Locate every blood parasite and identify its species.
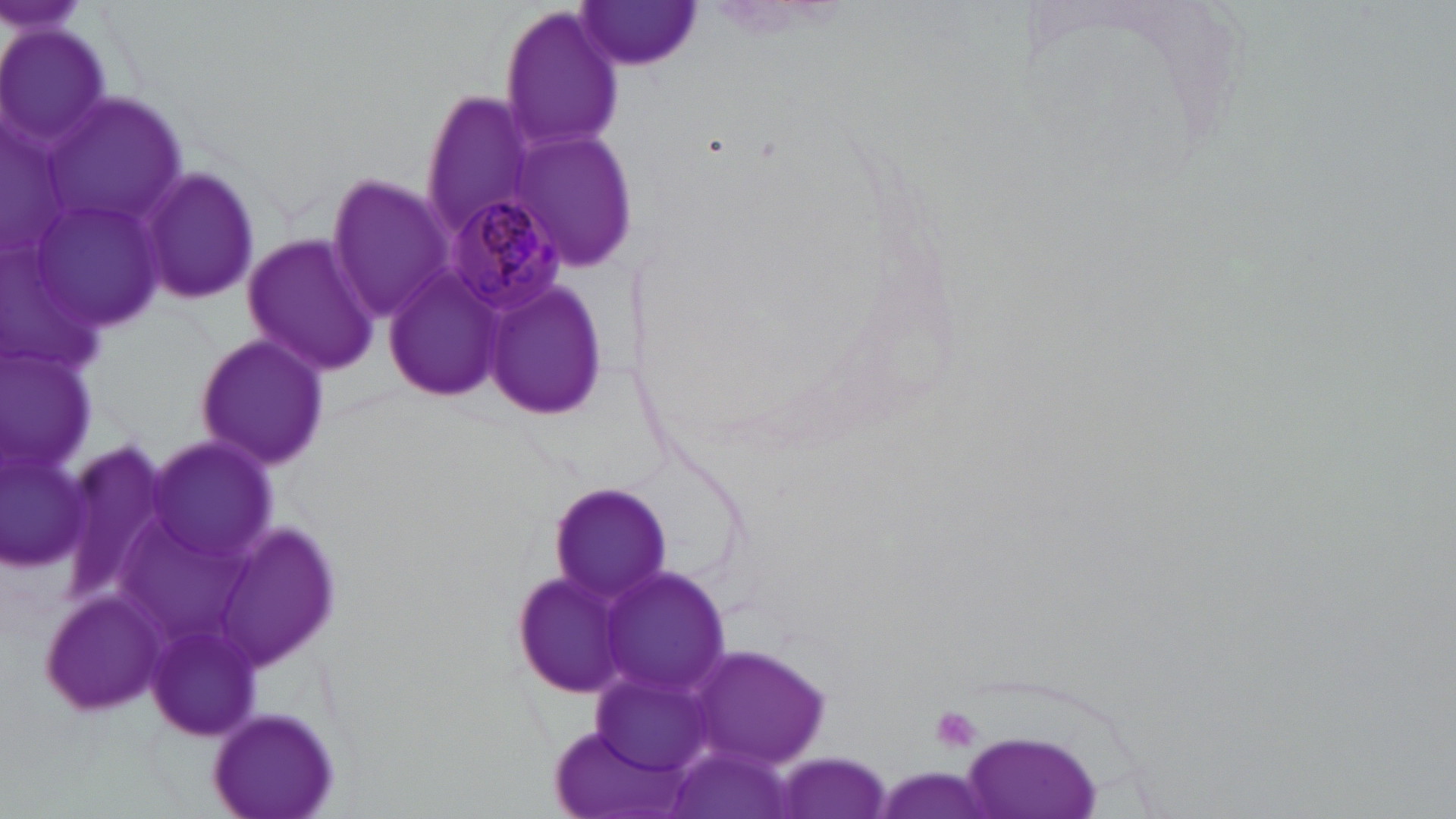

Approximate bounding boxes as (x1,y1)-(x2,y2) corner pairs in pixels.
Plasmodium malariae-infected red blood cells: (444,196)-(567,315).
No Plasmodium falciparum, Plasmodium ovale, Plasmodium vivax, Babesia divergens, or Trypanosoma brucei observed.

Summary:
  - Uninfected red blood cell locations: (576,1)-(705,71), (499,5)-(623,156), (0,23)-(118,158), (417,90)-(539,240), (47,94)-(191,230), (511,134)-(636,268), (139,165)-(260,308), (325,174)-(451,321), (240,232)-(379,377), (384,264)-(508,405), (482,278)-(608,421), (193,335)-(331,471), (1,347)-(98,481), (146,438)-(281,569), (4,448)-(92,569), (552,481)-(671,602), (217,521)-(348,668), (597,566)-(733,701), (510,568)-(632,698), (39,588)-(164,716), (689,644)-(834,770), (210,704)-(342,817), (956,729)-(1108,819), (669,743)-(797,819), (771,753)-(894,819)
  - Platelet locations: (929,703)-(984,754)
  - Slide-level diagnosis: Plasmodium malariae
  - Stain: May-Grünwald-Giemsa
  - Magnification: 1000x
  - Image size: 1456×819 pixels
  - Preparation: thin blood smear
  - Modality: light microscopy
  - Field of view: one of a larger specimen